Locate every Trypanosoma brucei.
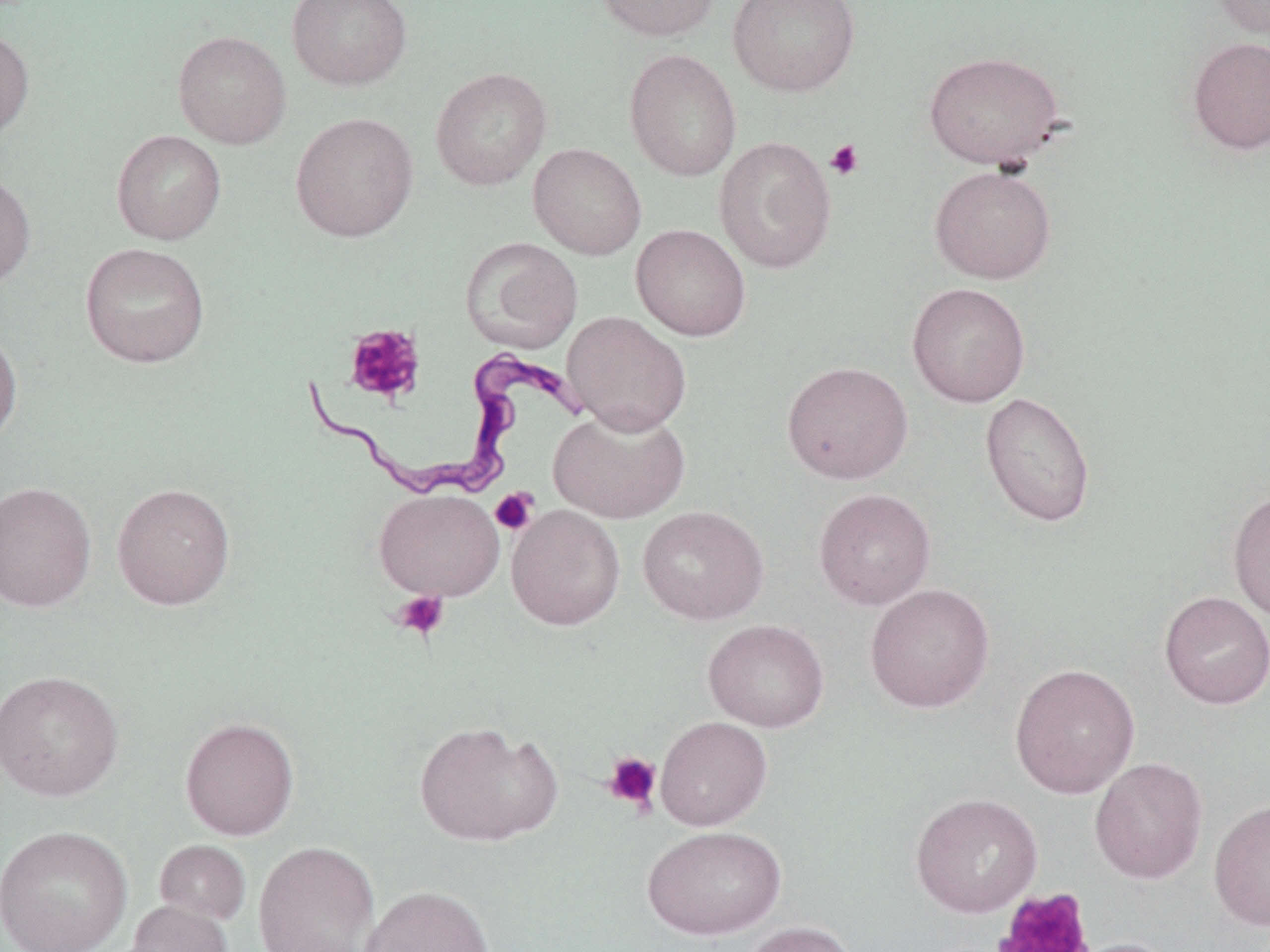
Approximate bounding boxes as (x1,y1)-(x2,y2) corner pairs in pixels.
Trypanosoma brucei: (302,348)-(590,503).

Uninfected red blood cell locations: (287,0)-(412,91), (593,0)-(721,41), (728,0)-(860,97), (1211,0)-(1269,39), (0,26)-(34,141), (173,30)-(292,149), (1186,36)-(1270,155), (624,49)-(742,181), (923,50)-(1065,169), (430,67)-(552,191), (290,111)-(419,242), (111,130)-(226,245), (714,136)-(837,274), (528,143)-(646,259), (929,165)-(1057,284), (0,171)-(36,289), (631,223)-(751,340), (460,237)-(583,354), (79,241)-(210,368), (906,282)-(1030,407), (562,311)-(692,435), (0,328)-(22,447), (781,361)-(913,484), (980,391)-(1096,528), (549,406)-(690,524), (0,481)-(97,612), (112,483)-(235,609), (374,488)-(505,601), (814,488)-(936,610), (1227,489)-(1270,623), (506,505)-(626,631), (637,506)-(769,624), (864,583)-(995,713), (1159,591)-(1270,709), (703,619)-(829,732), (1010,662)-(1140,798), (0,669)-(125,801), (179,716)-(300,840), (654,716)-(772,830), (413,719)-(561,847), (1089,757)-(1208,884), (910,792)-(1043,917), (1209,797)-(1270,930), (0,825)-(134,952), (642,825)-(786,939), (154,839)-(251,926), (253,841)-(380,952), (360,884)-(495,952), (125,900)-(233,951), (739,920)-(857,952), (1066,937)-(1183,952). Platelet locations: (825,139)-(865,181), (343,323)-(426,404), (490,488)-(539,536), (392,590)-(449,641), (602,751)-(662,813), (994,889)-(1095,952). Slide-level diagnosis: Trypanosoma brucei. Single field of view. Thin blood film. May-Grünwald-Giemsa stain. Image is 1270×952 pixels. 1000x magnification. Optical microscopy.